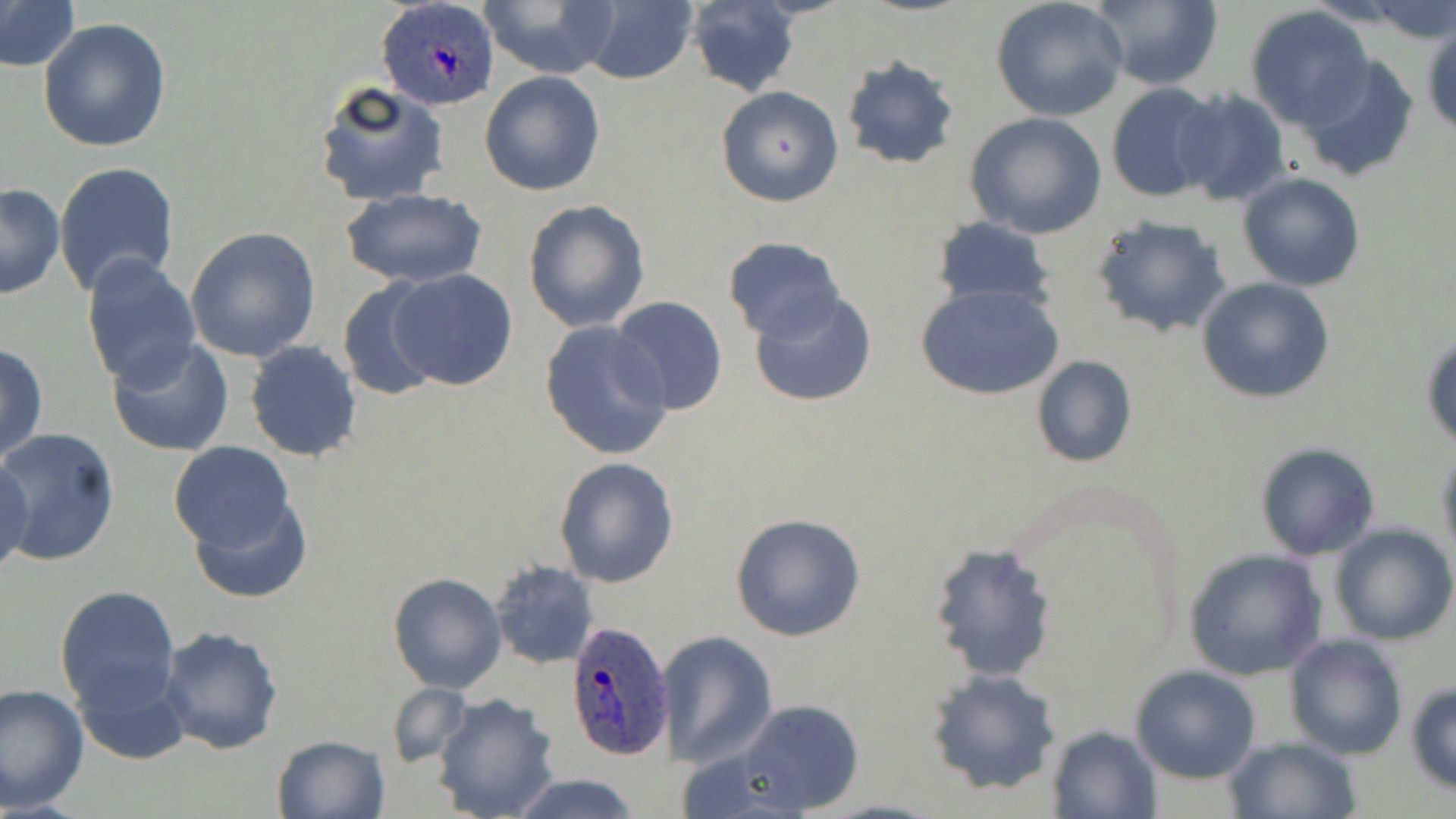
Summary:
  - Coordinate format: approximate bounding boxes as named x1/y1/x2/y2 corners in pixels
  - Plasmodium ovale-infected red blood cell locations: (x1=378, y1=0, x2=499, y2=112), (x1=563, y1=621, x2=675, y2=763)
  - Uninfected red blood cell locations: (x1=989, y1=0, x2=1129, y2=122), (x1=1087, y1=0, x2=1224, y2=91), (x1=0, y1=1, x2=80, y2=72), (x1=478, y1=1, x2=620, y2=78), (x1=578, y1=1, x2=699, y2=85), (x1=1372, y1=1, x2=1455, y2=45), (x1=683, y1=2, x2=801, y2=97), (x1=1245, y1=6, x2=1374, y2=130), (x1=38, y1=18, x2=171, y2=153), (x1=1423, y1=25, x2=1456, y2=136), (x1=840, y1=54, x2=961, y2=170), (x1=1295, y1=55, x2=1421, y2=184), (x1=480, y1=72, x2=605, y2=196), (x1=314, y1=81, x2=451, y2=206), (x1=1106, y1=82, x2=1226, y2=204), (x1=715, y1=85, x2=844, y2=208), (x1=1172, y1=87, x2=1291, y2=207), (x1=964, y1=112, x2=1107, y2=239), (x1=55, y1=161, x2=182, y2=297), (x1=1238, y1=172, x2=1367, y2=292), (x1=0, y1=183, x2=66, y2=298), (x1=342, y1=189, x2=488, y2=288), (x1=522, y1=199, x2=651, y2=333), (x1=1090, y1=213, x2=1232, y2=339), (x1=928, y1=217, x2=1057, y2=309), (x1=185, y1=227, x2=322, y2=362), (x1=722, y1=237, x2=846, y2=342), (x1=79, y1=254, x2=202, y2=390), (x1=388, y1=269, x2=520, y2=391), (x1=1196, y1=276, x2=1334, y2=404), (x1=335, y1=279, x2=443, y2=401), (x1=916, y1=282, x2=1066, y2=401), (x1=749, y1=290, x2=877, y2=408), (x1=607, y1=296, x2=729, y2=417), (x1=539, y1=321, x2=674, y2=461), (x1=1421, y1=327, x2=1455, y2=451), (x1=107, y1=336, x2=236, y2=458), (x1=0, y1=341, x2=49, y2=470), (x1=244, y1=341, x2=363, y2=461), (x1=1031, y1=356, x2=1137, y2=469), (x1=0, y1=428, x2=120, y2=567), (x1=167, y1=440, x2=297, y2=556), (x1=1254, y1=442, x2=1381, y2=561), (x1=1436, y1=448, x2=1456, y2=564), (x1=1, y1=455, x2=34, y2=579), (x1=553, y1=456, x2=680, y2=589), (x1=184, y1=490, x2=313, y2=604), (x1=730, y1=513, x2=866, y2=643), (x1=1330, y1=524, x2=1455, y2=645), (x1=929, y1=542, x2=1059, y2=682), (x1=1185, y1=549, x2=1327, y2=681), (x1=490, y1=559, x2=600, y2=670), (x1=388, y1=572, x2=508, y2=694), (x1=54, y1=585, x2=181, y2=715), (x1=157, y1=625, x2=285, y2=755), (x1=655, y1=630, x2=778, y2=767), (x1=1283, y1=633, x2=1408, y2=759), (x1=1129, y1=665, x2=1261, y2=785), (x1=71, y1=667, x2=189, y2=768), (x1=926, y1=668, x2=1061, y2=796), (x1=385, y1=682, x2=469, y2=770), (x1=1406, y1=682, x2=1456, y2=796), (x1=0, y1=683, x2=90, y2=813), (x1=431, y1=693, x2=564, y2=819), (x1=733, y1=699, x2=865, y2=816), (x1=1047, y1=725, x2=1162, y2=818), (x1=271, y1=733, x2=390, y2=819), (x1=1226, y1=736, x2=1359, y2=818), (x1=504, y1=771, x2=645, y2=819)
  - Slide-level diagnosis: Plasmodium ovale
  - Magnification: 1000x
  - Preparation: thin blood film
  - Modality: light microscopy
  - Stain: May-Grünwald-Giemsa
  - Field of view: single
  - Image size: 1456×819 pixels